Outline each Plasmodium falciparum-infected red blood cell.
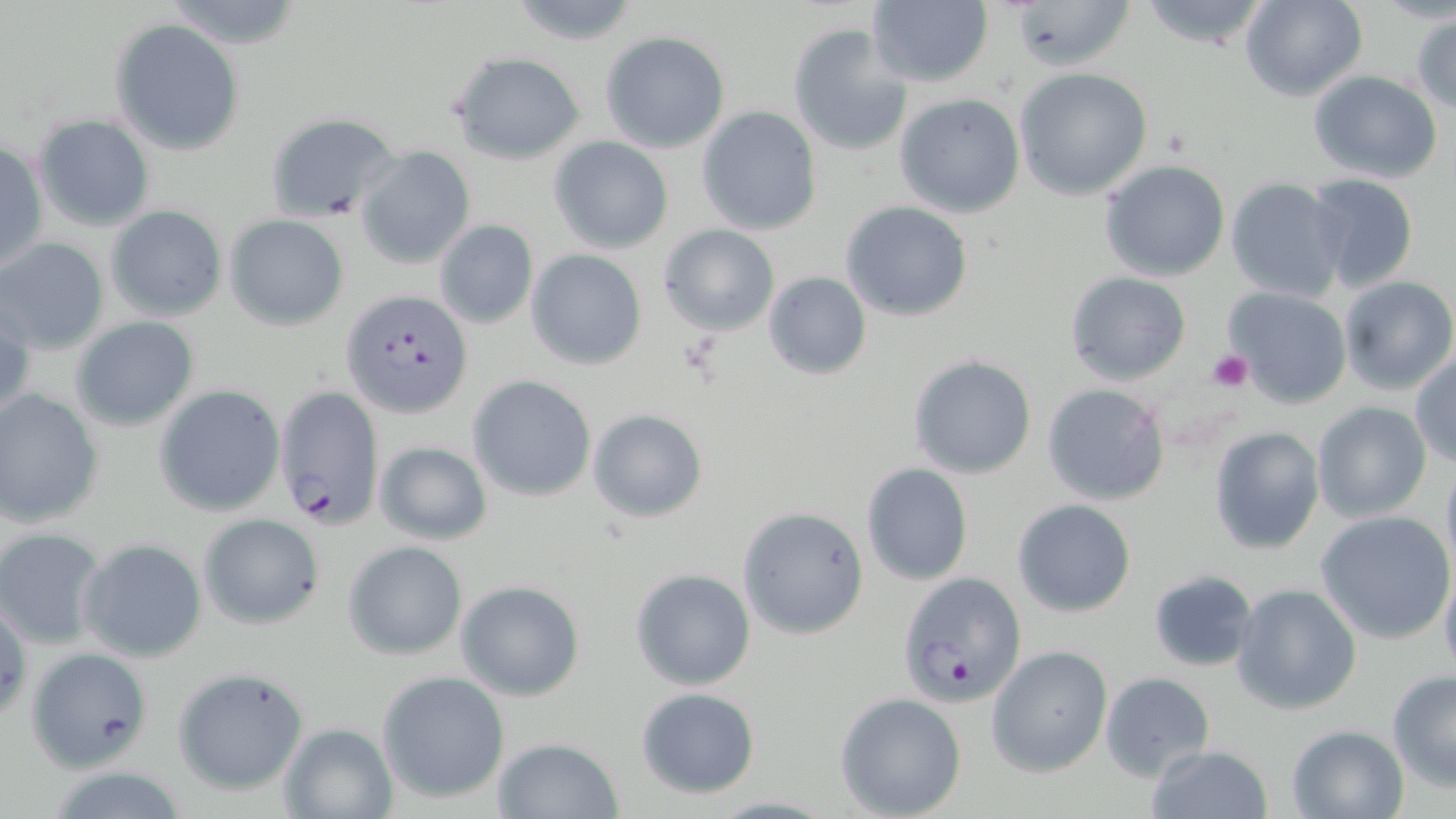
Approximate bounding boxes as [x1, y1, x2, y2] in pixels.
Plasmodium falciparum-infected red blood cells: [343, 289, 473, 419], [275, 386, 385, 530], [899, 573, 1026, 705].

Uninfected red blood cell locations: [505, 0, 647, 47], [1007, 0, 1136, 74], [1137, 0, 1275, 53], [1239, 0, 1369, 102], [865, 1, 994, 89], [1410, 12, 1456, 115], [110, 19, 244, 156], [789, 24, 911, 158], [599, 30, 731, 153], [451, 52, 585, 164], [1014, 67, 1153, 199], [1306, 71, 1443, 183], [893, 92, 1025, 218], [697, 106, 822, 235], [263, 109, 404, 227], [34, 114, 154, 232], [549, 136, 674, 254], [1, 139, 46, 274], [356, 146, 475, 270], [1099, 159, 1231, 282], [1303, 172, 1420, 290], [1226, 178, 1344, 302], [839, 199, 973, 322], [105, 206, 227, 321], [224, 215, 350, 330], [434, 219, 539, 328], [658, 224, 778, 335], [0, 237, 110, 352], [526, 249, 647, 370], [763, 271, 871, 380], [1065, 271, 1191, 386], [1336, 275, 1456, 395], [1224, 287, 1353, 408], [1, 292, 34, 422], [70, 316, 200, 432], [1409, 352, 1456, 468], [907, 354, 1039, 480], [468, 376, 597, 501], [1042, 383, 1169, 505], [154, 385, 285, 515], [0, 389, 104, 527], [1312, 401, 1432, 522], [588, 408, 709, 523], [1208, 425, 1326, 554], [373, 440, 492, 545], [1440, 459, 1456, 577], [861, 463, 973, 585], [1012, 498, 1137, 616], [738, 505, 869, 640], [1317, 511, 1454, 642], [200, 514, 324, 628], [0, 526, 108, 651], [78, 538, 207, 664], [343, 540, 467, 660], [630, 566, 755, 691], [1439, 566, 1456, 682], [1148, 568, 1259, 671], [455, 579, 585, 702], [1231, 584, 1363, 715], [987, 646, 1112, 777], [27, 647, 153, 770], [173, 667, 309, 797], [1100, 670, 1214, 781], [1386, 670, 1456, 792], [376, 671, 510, 804], [635, 686, 761, 798], [835, 692, 967, 818], [278, 722, 399, 818], [1285, 724, 1410, 818], [491, 737, 625, 818], [1144, 745, 1274, 819], [704, 794, 837, 817]. Platelet locations: [1208, 348, 1253, 391]. Slide-level diagnosis: Plasmodium falciparum. Light microscopy. Thin blood smear. Image is 1456×819 pixels. Captured at 1000x magnification. One field of a larger specimen. May-Grünwald-Giemsa-stained preparation.